Outline each blood parasite and name the species.
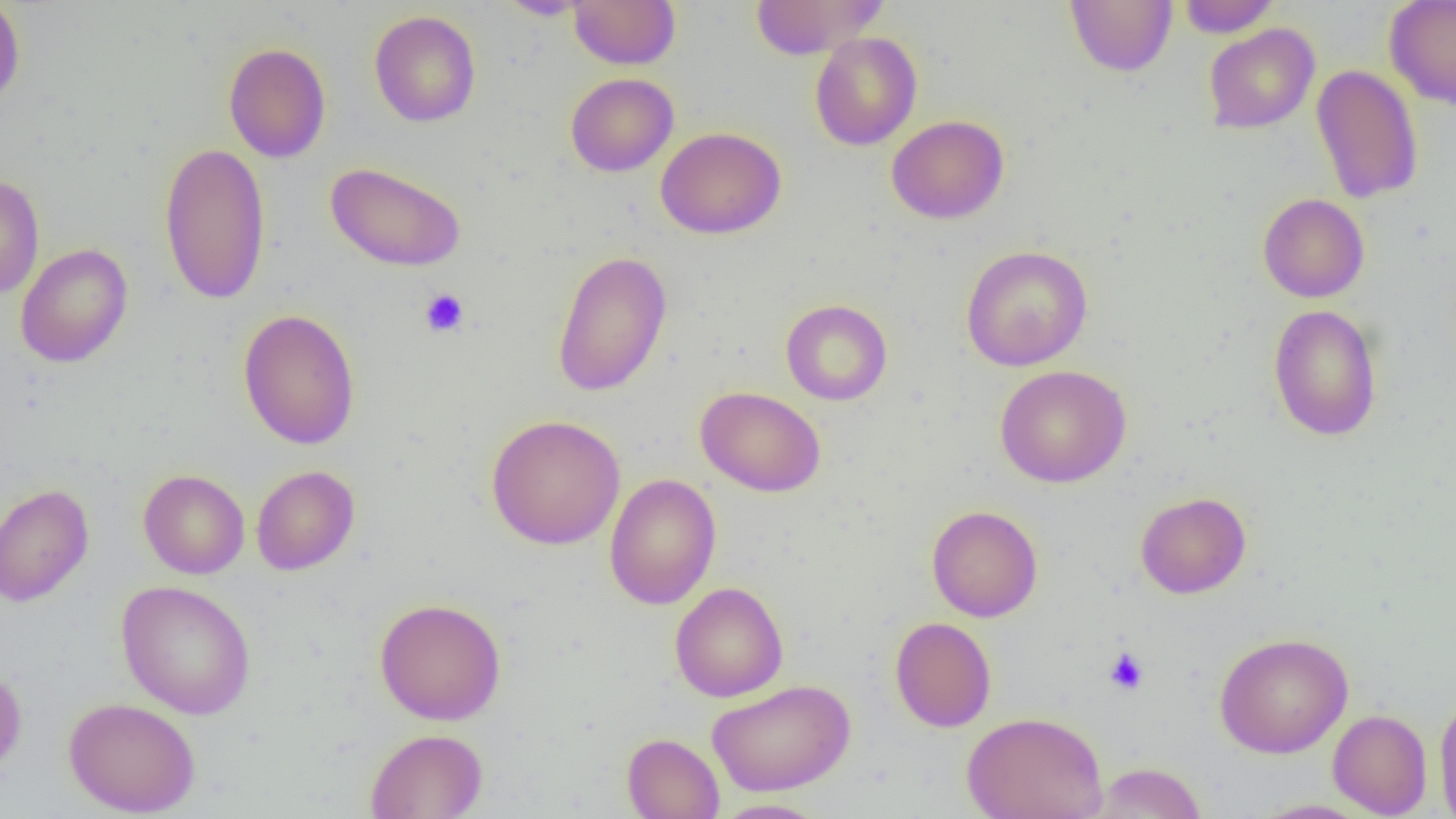
No blood parasites observed.

slide-level diagnosis = negative for blood parasites
uninfected red blood cell locations = approximate bounding boxes as (x1, y1, x2, y2) in pixels: (0, 0, 26, 108), (495, 0, 592, 20), (568, 0, 681, 69), (748, 0, 884, 59), (1065, 0, 1177, 77), (1177, 0, 1281, 37), (1384, 0, 1456, 111), (369, 10, 481, 127), (1203, 23, 1319, 134), (809, 31, 923, 151), (223, 42, 331, 163), (1311, 63, 1424, 204), (566, 72, 679, 176), (887, 115, 1009, 224), (656, 126, 786, 239), (159, 141, 271, 305), (325, 162, 466, 272), (0, 173, 45, 299), (1258, 193, 1370, 303), (15, 243, 134, 368), (961, 245, 1093, 370), (552, 250, 672, 397), (780, 299, 892, 406), (1267, 304, 1383, 441), (238, 308, 361, 449), (995, 365, 1131, 488), (696, 386, 827, 497), (486, 414, 625, 550), (251, 465, 359, 575), (138, 469, 250, 579), (604, 473, 722, 610), (0, 483, 95, 606), (1135, 491, 1251, 599), (926, 504, 1043, 622), (116, 580, 256, 720), (670, 582, 788, 702), (374, 597, 506, 725), (890, 616, 996, 732), (1214, 632, 1353, 758), (0, 664, 27, 776), (706, 679, 855, 796), (1434, 689, 1456, 819), (63, 696, 201, 817), (1328, 709, 1432, 817), (961, 710, 1109, 819), (365, 728, 488, 819), (621, 733, 724, 819), (1091, 761, 1208, 818), (710, 798, 832, 818), (1250, 798, 1376, 818)
image size = 1456×819 pixels
magnification = 1000x
field of view = one of a larger specimen
modality = optical microscopy
platelet locations = approximate bounding boxes as (x1, y1, x2, y2) in pixels: (419, 288, 469, 337), (1104, 647, 1150, 695)
preparation = thin blood film